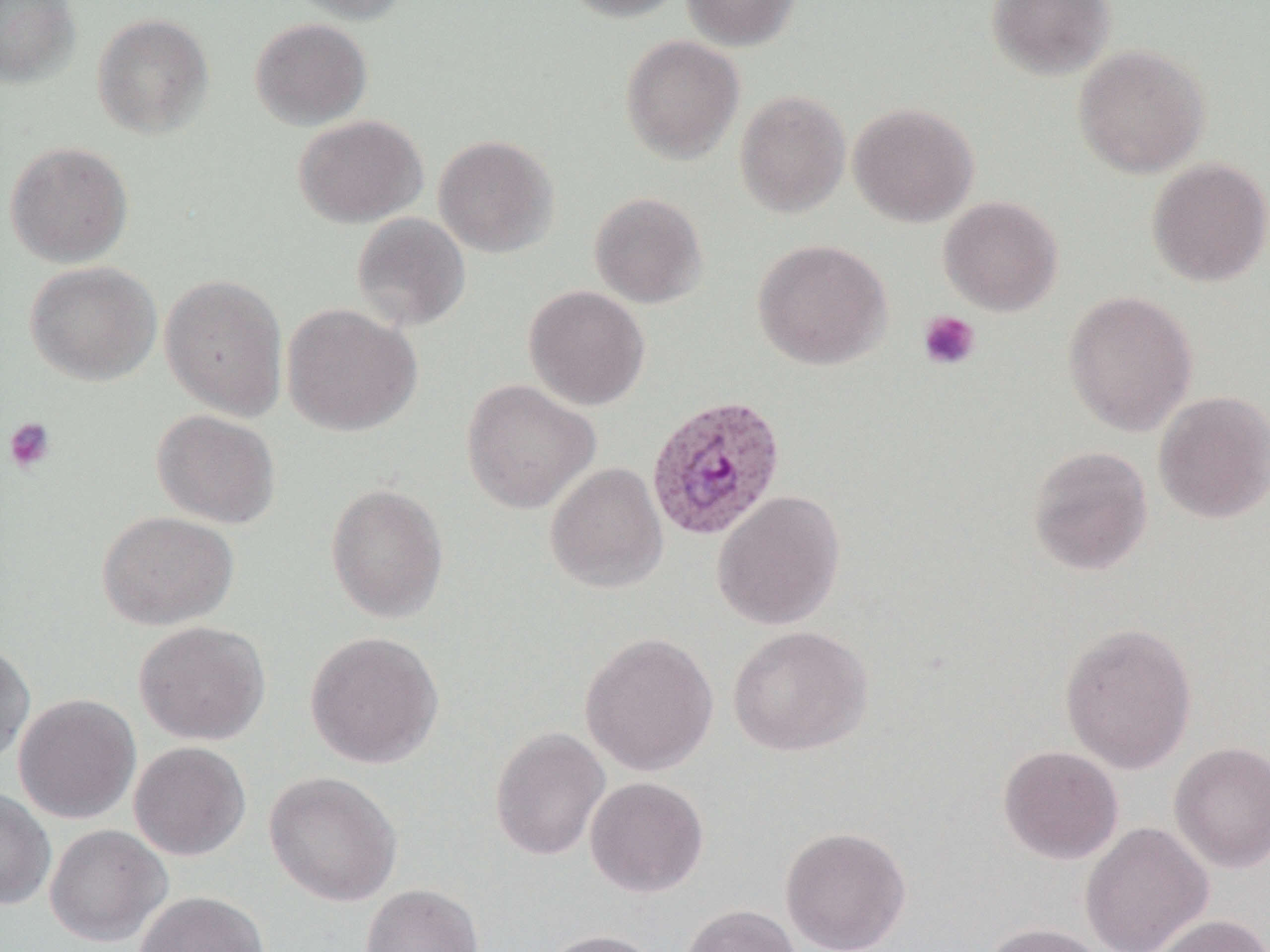
slide-level diagnosis = Plasmodium ovale
preparation = thin blood film
field of view = one of a larger specimen
uninfected red blood cell locations = approximate bounding boxes as (x1,y1)-(x2,y2) corner pairs in pixels: (0,0)-(81,88), (278,0)-(412,24), (558,0)-(689,21), (682,0)-(801,51), (987,0)-(1115,80), (91,12)-(214,139), (249,17)-(373,130), (620,35)-(745,164), (1073,44)-(1210,178), (734,91)-(851,218), (848,102)-(979,227), (293,114)-(428,227), (433,134)-(560,258), (5,141)-(134,268), (1148,158)-(1270,287), (589,192)-(708,308), (938,196)-(1064,316), (351,212)-(471,332), (752,239)-(892,370), (25,261)-(162,386), (160,274)-(290,420), (524,285)-(650,410), (1063,289)-(1198,436), (282,303)-(422,436), (461,379)-(600,514), (1154,390)-(1270,524), (151,409)-(281,529), (1027,445)-(1153,576), (545,462)-(668,594), (325,483)-(449,623), (712,490)-(846,631), (97,510)-(239,630), (133,620)-(271,745), (1059,621)-(1198,774), (727,625)-(873,757), (305,631)-(444,769), (579,631)-(719,776), (0,640)-(35,768), (14,693)-(140,824), (489,726)-(610,861), (129,741)-(251,861), (1169,741)-(1270,873), (997,744)-(1123,865), (264,770)-(403,906), (584,776)-(709,897), (0,787)-(56,910), (1080,822)-(1214,952), (45,824)-(172,947), (780,826)-(912,952), (360,883)-(485,952), (134,890)-(270,952), (680,904)-(803,952), (1148,914)-(1270,952), (979,921)-(1112,952), (539,928)-(666,952)
platelet locations = approximate bounding boxes as (x1,y1)-(x2,y2) corner pairs in pixels: (918,311)-(981,371), (4,417)-(56,474)
Plasmodium ovale-infected red blood cell locations = approximate bounding boxes as (x1,y1)-(x2,y2) corner pairs in pixels: (646,394)-(786,541)
modality = optical microscopy
magnification = 1000x
image size = 1270×952 pixels